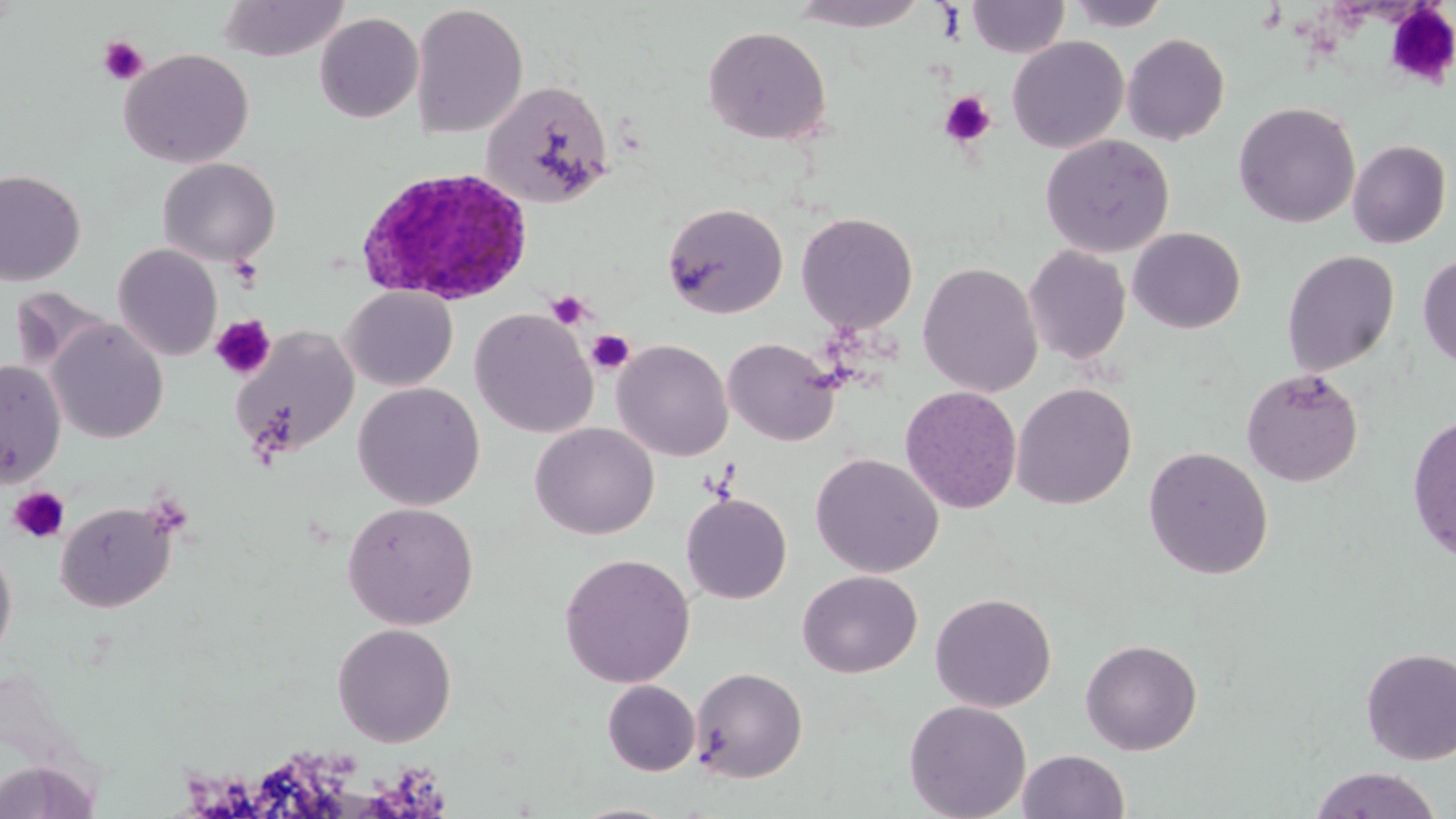
slide_level_diagnosis: Plasmodium ovale
modality: optical microscopy
plasmodium_ovale_infected_red_blood_cell_locations: 'approximate bounding boxes as [x1, y1, x2, y2] in pixels: [354, 166, 535, 307]'
stain: May-Grünwald-Giemsa
uninfected_red_blood_cell_locations: 'approximate bounding boxes as [x1, y1, x2, y2] in pixels: [217, 0, 350, 62], [790, 0, 929, 31], [967, 0, 1071, 58], [1066, 0, 1173, 31], [410, 3, 528, 139], [314, 12, 424, 123], [702, 25, 832, 144], [1121, 33, 1230, 145], [1006, 36, 1129, 153], [118, 48, 254, 169], [480, 80, 615, 208], [1233, 102, 1360, 228], [1039, 133, 1175, 257], [1348, 139, 1452, 249], [157, 157, 281, 266], [0, 170, 85, 286], [661, 201, 788, 319], [795, 211, 918, 334], [1128, 227, 1246, 333], [113, 243, 222, 361], [1023, 244, 1131, 365], [1281, 250, 1400, 376], [1418, 253, 1456, 369], [918, 261, 1043, 397], [12, 287, 112, 374], [341, 287, 458, 391], [470, 308, 598, 438], [47, 319, 168, 444], [229, 326, 360, 460], [723, 336, 841, 447], [612, 339, 733, 462], [0, 359, 66, 488], [1241, 368, 1364, 487], [352, 382, 486, 511], [1011, 382, 1137, 510], [900, 385, 1022, 514], [1405, 411, 1456, 565], [530, 423, 659, 539], [1143, 446, 1273, 580], [809, 452, 944, 577], [681, 493, 792, 604], [55, 500, 176, 612], [342, 501, 479, 630], [0, 541, 17, 666], [558, 552, 695, 688], [797, 570, 922, 677], [930, 592, 1057, 712], [331, 623, 457, 747], [1080, 638, 1203, 755], [1360, 647, 1456, 764], [690, 666, 808, 783], [602, 680, 701, 775], [903, 699, 1032, 819], [1017, 749, 1130, 818], [0, 760, 99, 818], [1308, 766, 1444, 819], [567, 802, 683, 819]'
image_size: 1456×819 pixels
platelet_locations: 'approximate bounding boxes as [x1, y1, x2, y2] in pixels: [1384, 3, 1456, 90], [98, 36, 149, 86], [939, 90, 996, 148], [546, 289, 593, 330], [210, 314, 276, 380], [585, 329, 635, 375], [8, 487, 70, 543]'
magnification: 1000x
preparation: thin blood smear
field_of_view: one of a larger specimen